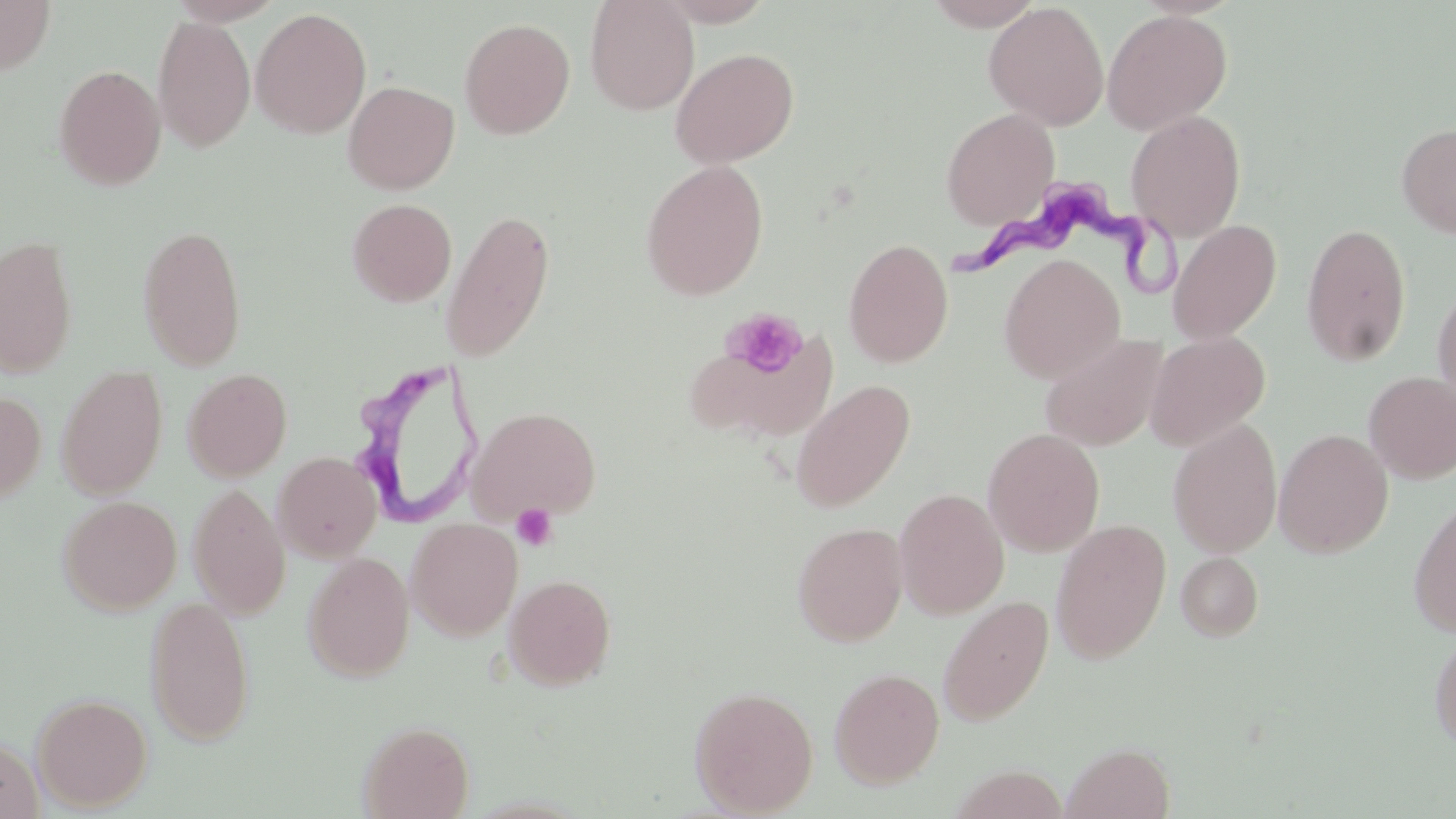
Summary:
  - Coordinate format: approximate bounding boxes as named x1/y1/x2/y2 corners in pixels
  - Trypanosoma brucei locations: (x1=942, y1=184, x2=1180, y2=302), (x1=347, y1=360, x2=485, y2=525)
  - Uninfected red blood cell locations: (x1=167, y1=0, x2=284, y2=26), (x1=584, y1=0, x2=700, y2=115), (x1=655, y1=0, x2=775, y2=26), (x1=923, y1=0, x2=1044, y2=30), (x1=1, y1=1, x2=56, y2=76), (x1=983, y1=1, x2=1110, y2=130), (x1=250, y1=7, x2=372, y2=139), (x1=1102, y1=9, x2=1232, y2=134), (x1=152, y1=15, x2=256, y2=153), (x1=459, y1=17, x2=576, y2=139), (x1=670, y1=47, x2=800, y2=168), (x1=53, y1=64, x2=167, y2=191), (x1=343, y1=80, x2=459, y2=194), (x1=940, y1=107, x2=1060, y2=231), (x1=1126, y1=111, x2=1246, y2=242), (x1=1396, y1=122, x2=1456, y2=238), (x1=640, y1=160, x2=769, y2=301), (x1=346, y1=198, x2=457, y2=307), (x1=440, y1=209, x2=556, y2=363), (x1=1168, y1=219, x2=1281, y2=343), (x1=1301, y1=223, x2=1412, y2=367), (x1=137, y1=224, x2=248, y2=371), (x1=0, y1=234, x2=79, y2=378), (x1=843, y1=238, x2=953, y2=367), (x1=998, y1=253, x2=1125, y2=382), (x1=1432, y1=280, x2=1456, y2=417), (x1=1145, y1=331, x2=1270, y2=450), (x1=1039, y1=333, x2=1168, y2=451), (x1=694, y1=340, x2=846, y2=438), (x1=56, y1=365, x2=168, y2=499), (x1=182, y1=367, x2=293, y2=482), (x1=1363, y1=372, x2=1456, y2=484), (x1=791, y1=379, x2=915, y2=512), (x1=0, y1=391, x2=46, y2=505), (x1=469, y1=406, x2=601, y2=522), (x1=1167, y1=418, x2=1282, y2=558), (x1=983, y1=428, x2=1105, y2=557), (x1=1274, y1=429, x2=1393, y2=558), (x1=273, y1=451, x2=382, y2=562), (x1=188, y1=484, x2=291, y2=618), (x1=894, y1=488, x2=1009, y2=619), (x1=58, y1=495, x2=182, y2=615), (x1=1408, y1=496, x2=1456, y2=638), (x1=406, y1=517, x2=523, y2=640), (x1=1050, y1=519, x2=1171, y2=664), (x1=792, y1=522, x2=908, y2=646), (x1=302, y1=552, x2=414, y2=682), (x1=1176, y1=552, x2=1264, y2=641), (x1=503, y1=573, x2=616, y2=690), (x1=144, y1=594, x2=256, y2=746), (x1=938, y1=596, x2=1053, y2=726), (x1=1428, y1=626, x2=1456, y2=752), (x1=829, y1=667, x2=945, y2=788), (x1=689, y1=685, x2=819, y2=816), (x1=31, y1=692, x2=153, y2=811), (x1=358, y1=720, x2=475, y2=819), (x1=0, y1=735, x2=44, y2=818), (x1=1062, y1=742, x2=1175, y2=819)
  - Platelet locations: (x1=722, y1=308, x2=809, y2=379), (x1=511, y1=504, x2=558, y2=551)
  - Slide-level diagnosis: Trypanosoma brucei
  - Magnification: 1000x
  - Image size: 1456×819 pixels
  - Modality: light microscopy
  - Preparation: thin blood film
  - Stain: May-Grünwald-Giemsa
  - Field of view: single